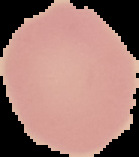
preparation = thin blood smear
image type = segmented cell region on a black background
result = no Plasmodium parasites detected
image size = 139×157 pixels